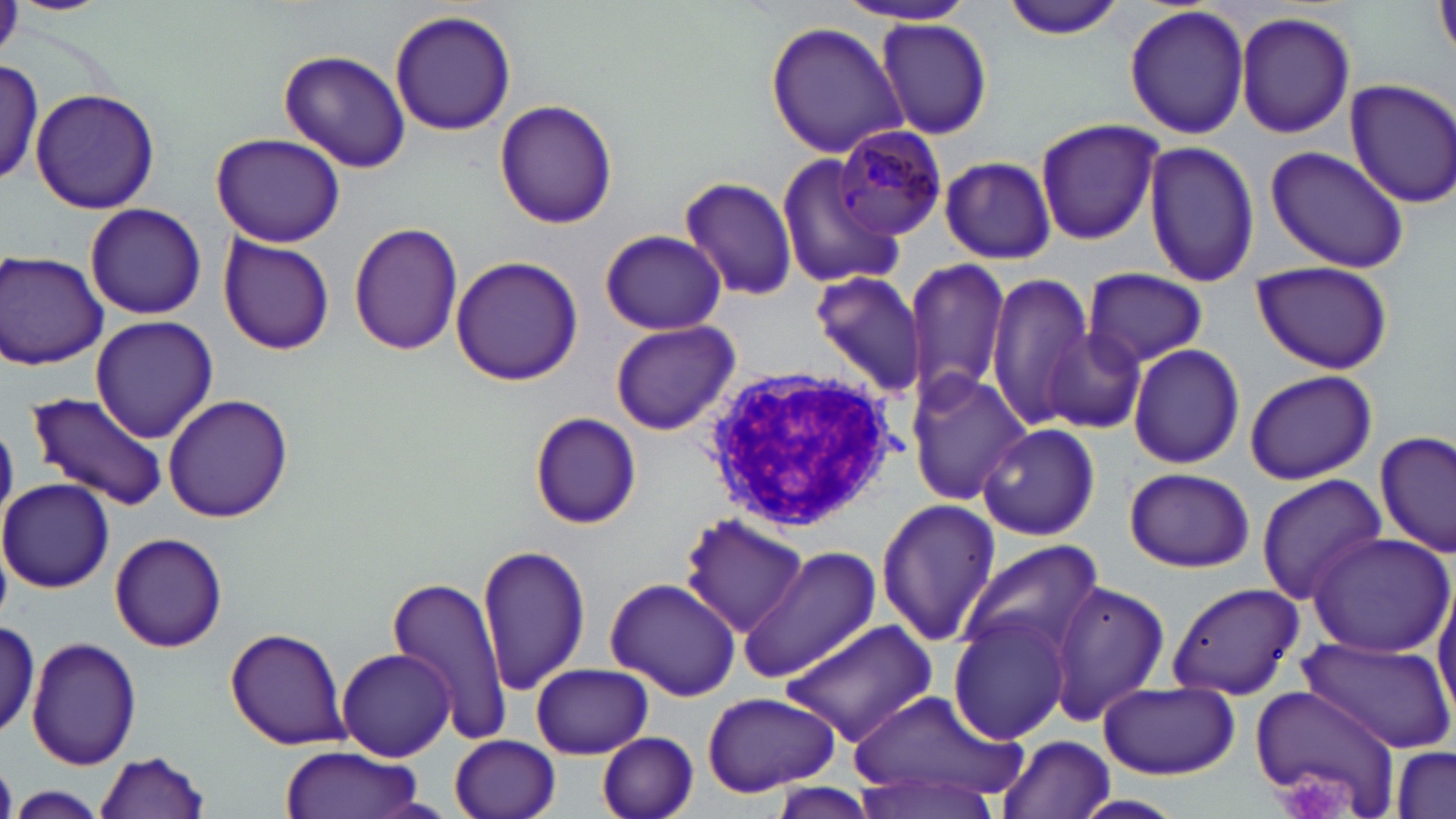
slide-level diagnosis = Plasmodium malariae
platelet locations = approximate bounding boxes as (x1,y1)-(x2,y2) corner pairs in pixels: (1269,771)-(1354,817)
preparation = thin blood film
field of view = one of a larger specimen
uninfected red blood cell locations = approximate bounding boxes as (x1,y1)-(x2,y2) corner pairs in pixels: (999,0)-(1132,40), (832,2)-(980,26), (1123,4)-(1250,140), (390,8)-(517,137), (1234,11)-(1357,139), (877,18)-(993,140), (766,20)-(908,159), (278,48)-(410,175), (0,61)-(53,194), (1345,78)-(1456,209), (32,89)-(159,213), (494,99)-(618,230), (1034,119)-(1162,246), (209,133)-(346,247), (1143,139)-(1260,288), (1264,144)-(1411,273), (776,154)-(899,288), (938,155)-(1059,264), (682,175)-(801,301), (84,204)-(207,320), (350,222)-(464,358), (599,229)-(727,336), (219,233)-(335,355), (1,251)-(109,371), (450,258)-(585,388), (904,259)-(1012,400), (1249,261)-(1394,375), (1082,268)-(1208,367), (810,270)-(926,395), (986,276)-(1093,431), (91,316)-(220,444), (610,320)-(740,436), (1043,326)-(1148,435), (1128,343)-(1245,469), (1243,369)-(1378,484), (905,370)-(1030,506), (27,392)-(169,509), (164,395)-(294,522), (529,412)-(643,530), (977,424)-(1100,540), (1375,430)-(1455,557), (1123,467)-(1253,572), (1256,475)-(1388,604), (1,478)-(114,593), (876,498)-(1000,648), (680,515)-(809,638), (1304,530)-(1454,659), (110,534)-(227,652), (959,539)-(1101,671), (477,543)-(591,695), (739,545)-(881,682), (385,574)-(514,748), (605,577)-(740,702), (1167,580)-(1305,701), (1047,581)-(1169,725), (1434,583)-(1456,721), (949,612)-(1074,744), (1,617)-(41,738), (783,621)-(938,744), (226,627)-(349,750), (1297,635)-(1454,752), (27,637)-(142,771), (337,646)-(456,761), (531,663)-(652,758), (1097,680)-(1238,779), (1247,685)-(1402,818), (844,689)-(1025,812), (701,692)-(842,798), (597,732)-(699,819), (451,734)-(561,819), (997,734)-(1117,819), (279,745)-(427,819), (1389,745)-(1453,819), (95,751)-(210,817), (851,768)-(1007,819), (9,787)-(108,818), (1072,793)-(1187,819)
magnification = 1000x
modality = optical microscopy
white blood cell locations = approximate bounding boxes as (x1,y1)-(x2,y2) corner pairs in pixels: (700,364)-(897,530)
Plasmodium malariae-infected red blood cell locations = approximate bounding boxes as (x1,y1)-(x2,y2) corner pairs in pixels: (832,124)-(946,241)
stain = May-Grünwald-Giemsa
image size = 1456×819 pixels